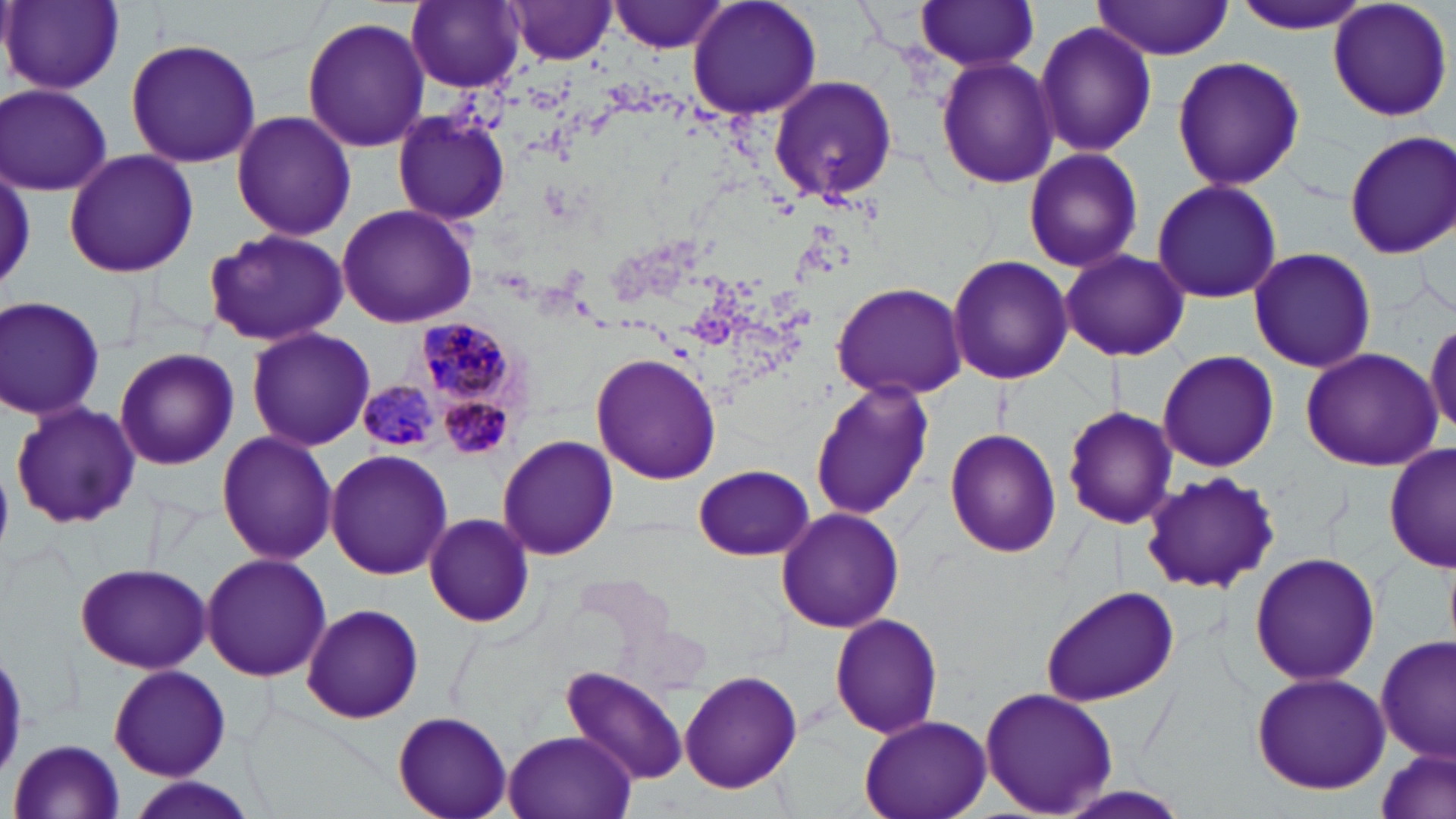
Approximate bounding boxes as [x1, y1, x2, y2] in pixels. Uninfected red blood cell locations: [611, 0, 730, 54], [688, 0, 821, 122], [1230, 0, 1374, 34], [1326, 0, 1453, 122], [4, 1, 124, 93], [407, 1, 525, 92], [914, 1, 1042, 74], [1091, 1, 1235, 59], [505, 2, 618, 66], [301, 16, 432, 153], [1036, 21, 1156, 158], [124, 38, 261, 168], [1170, 56, 1305, 191], [937, 59, 1059, 190], [768, 75, 898, 204], [2, 85, 113, 195], [392, 108, 511, 223], [230, 110, 357, 242], [1344, 130, 1456, 257], [1023, 146, 1143, 273], [61, 148, 200, 281], [1152, 178, 1283, 305], [336, 203, 479, 327], [203, 228, 349, 347], [1247, 247, 1378, 374], [1060, 249, 1190, 362], [947, 254, 1073, 387], [830, 280, 968, 400], [0, 296, 106, 421], [1425, 316, 1456, 441], [246, 326, 374, 451], [114, 347, 239, 470], [1300, 348, 1442, 469], [1158, 351, 1279, 471], [591, 352, 723, 485], [811, 382, 937, 521], [9, 399, 142, 530], [1062, 406, 1177, 531], [216, 429, 337, 565], [945, 429, 1061, 558], [497, 435, 619, 560], [1384, 444, 1455, 576], [324, 449, 453, 580], [694, 464, 813, 560], [1137, 470, 1280, 593], [776, 506, 905, 633], [423, 513, 535, 627], [1248, 551, 1382, 688], [199, 553, 331, 683], [74, 560, 212, 675], [1040, 585, 1178, 707], [300, 604, 427, 724], [829, 612, 944, 739], [1376, 636, 1452, 762], [109, 666, 231, 782], [562, 666, 689, 787], [678, 670, 804, 792], [1251, 671, 1391, 793], [979, 686, 1117, 816], [392, 710, 514, 819], [859, 714, 992, 819], [503, 730, 636, 819], [10, 738, 126, 819], [1375, 746, 1454, 819], [129, 778, 259, 819]. Plasmodium malariae-infected red blood cell locations: [420, 322, 517, 400], [357, 382, 440, 451], [442, 399, 509, 457]. Slide-level diagnosis: Plasmodium malariae. Image is 1456×819 pixels. Thin blood smear. Light microscopy. 1000x magnification. One field of a larger specimen. May-Grünwald-Giemsa-stained preparation.